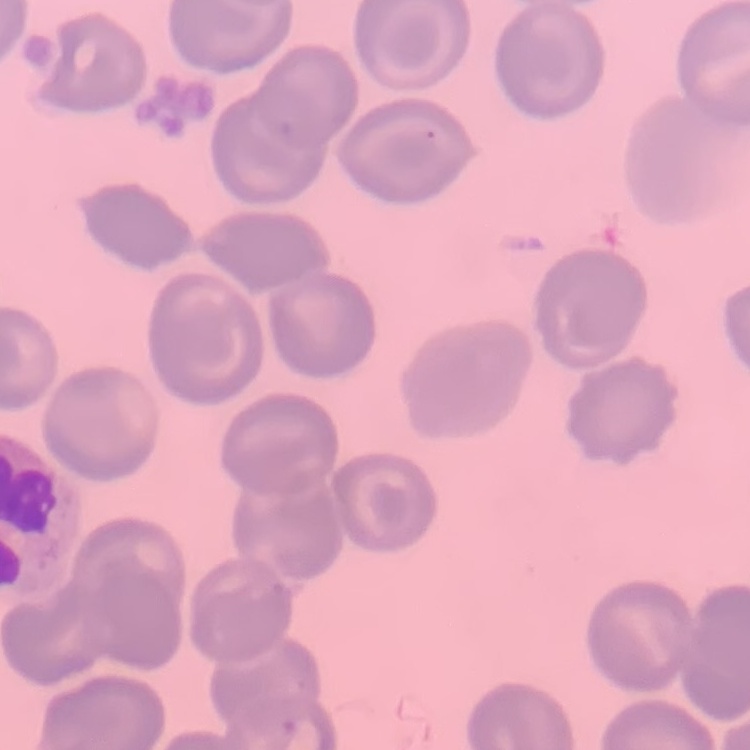
erythrocyte_morphology: no rouleaux formation
image_type: one tile cut from a larger photomicrograph
stain: Field's or Giemsa
preparation: thin peripheral smear